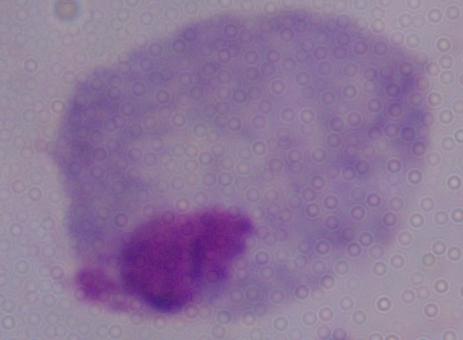
Summary:
  - Identification: trichomonad
  - Magnification: 1000x
  - Modality: micrograph